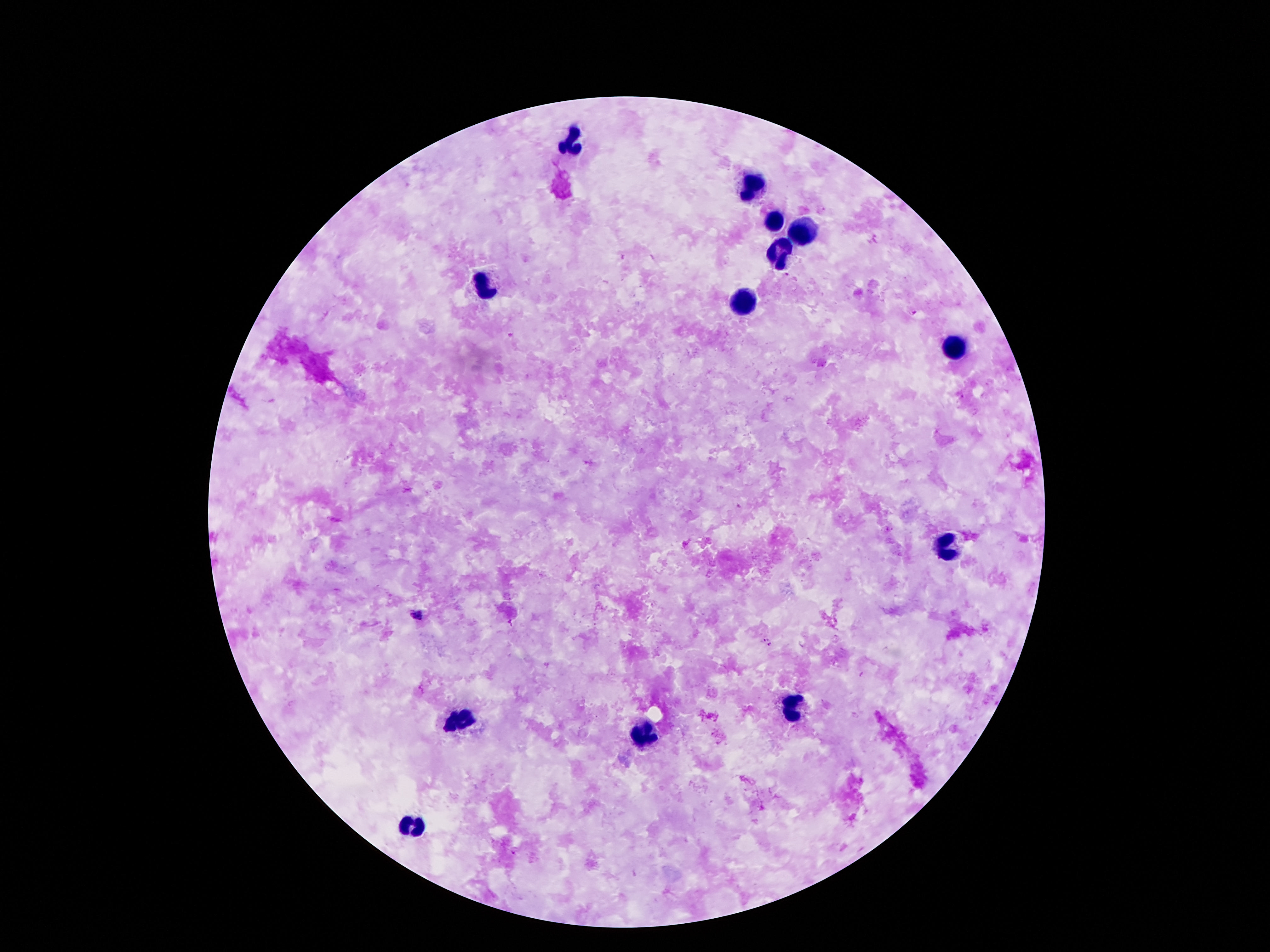 Approximate centers as {x, y} in pixels. Leukocyte locations: {570, 141}, {752, 185}, {773, 222}, {806, 232}, {778, 258}, {484, 288}, {743, 303}, {951, 348}, {948, 545}, {790, 709}, {458, 722}, {645, 736}, {414, 823}. Smartphone photograph taken through the microscope eyepiece. One field from this slide. Image is 1270×952 pixels. 100x magnification. Thick blood smear. Patient malaria status: not infected. Giemsa stain.